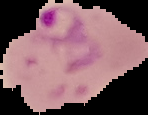

preparation = thin blood film
image type = segmented cell region with the area outside set to black
result = malaria parasites detected
image size = 148×115 pixels